Locate every Plasmodium falciparum-infected red blood cell.
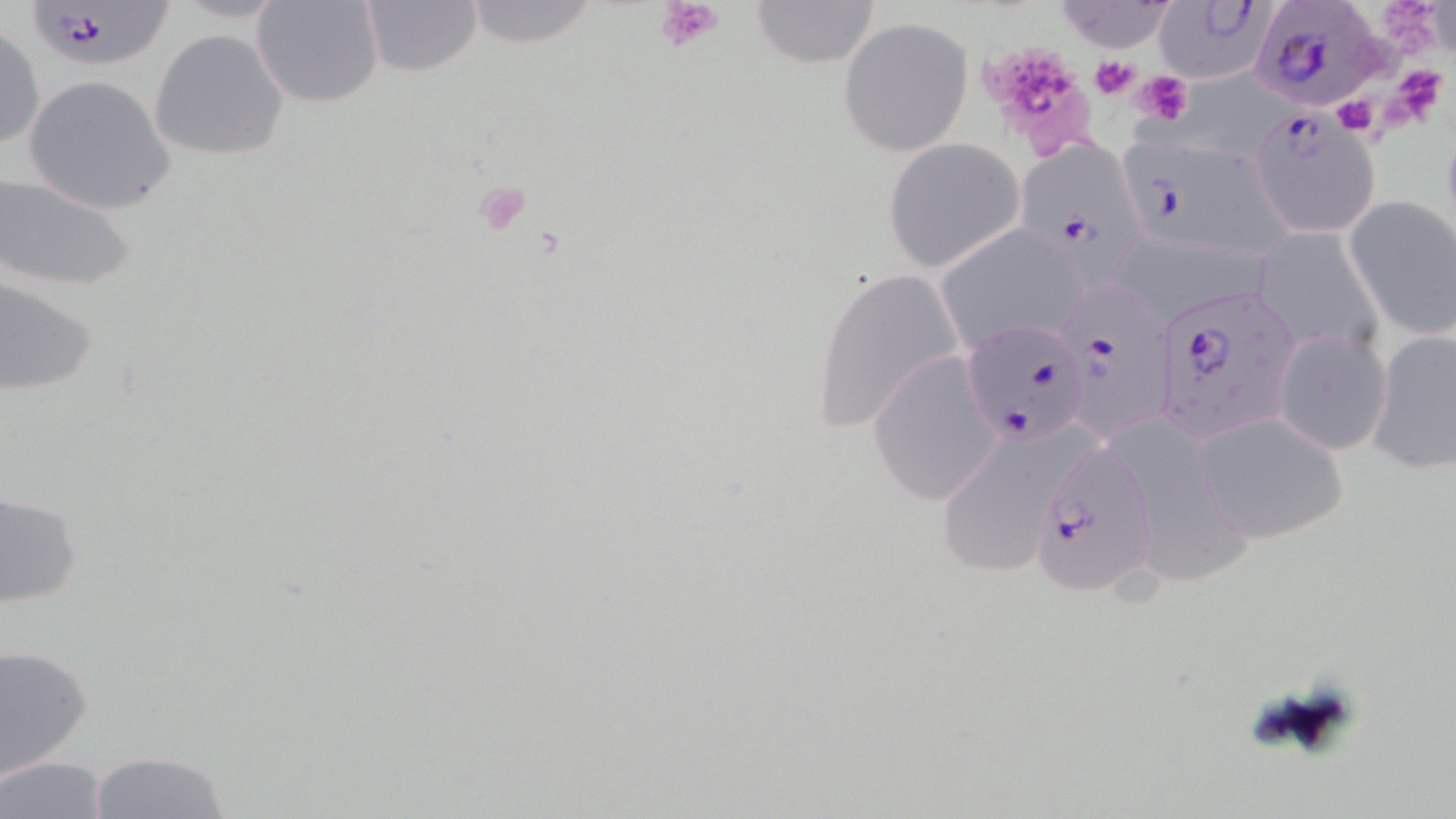

Approximate bounding boxes as [x1, y1, x2, y2] in pixels.
Plasmodium falciparum-infected red blood cells: [1155, 0, 1272, 84], [19, 1, 179, 72], [1251, 2, 1386, 109], [1247, 108, 1381, 239], [1122, 136, 1291, 263], [1016, 140, 1147, 268], [1055, 284, 1174, 446], [1151, 285, 1300, 446], [960, 316, 1089, 448], [1028, 440, 1160, 603].

Uninfected red blood cell locations: [251, 0, 385, 110], [359, 0, 482, 78], [748, 0, 881, 69], [1054, 0, 1180, 53], [462, 1, 605, 50], [837, 17, 974, 157], [0, 21, 45, 152], [150, 28, 289, 162], [24, 74, 178, 216], [882, 139, 1025, 272], [2, 172, 138, 292], [1345, 195, 1456, 340], [935, 223, 1087, 352], [1254, 228, 1383, 356], [809, 269, 963, 434], [0, 277, 99, 396], [1366, 327, 1456, 475], [1272, 328, 1392, 457], [867, 352, 1003, 507], [1192, 410, 1349, 546], [942, 438, 1081, 579], [1122, 445, 1252, 591], [0, 491, 82, 609], [1, 642, 96, 779], [91, 750, 232, 819], [1, 756, 110, 819]. Platelet locations: [655, 0, 724, 55], [977, 38, 1101, 163], [1092, 55, 1141, 100], [1135, 70, 1192, 124], [1332, 92, 1380, 135], [471, 180, 532, 236]. Slide-level diagnosis: Plasmodium falciparum. 1000x magnification. Light microscopy. May-Grünwald-Giemsa stain. Thin blood film. One field of a larger specimen. Image is 1456×819 pixels.